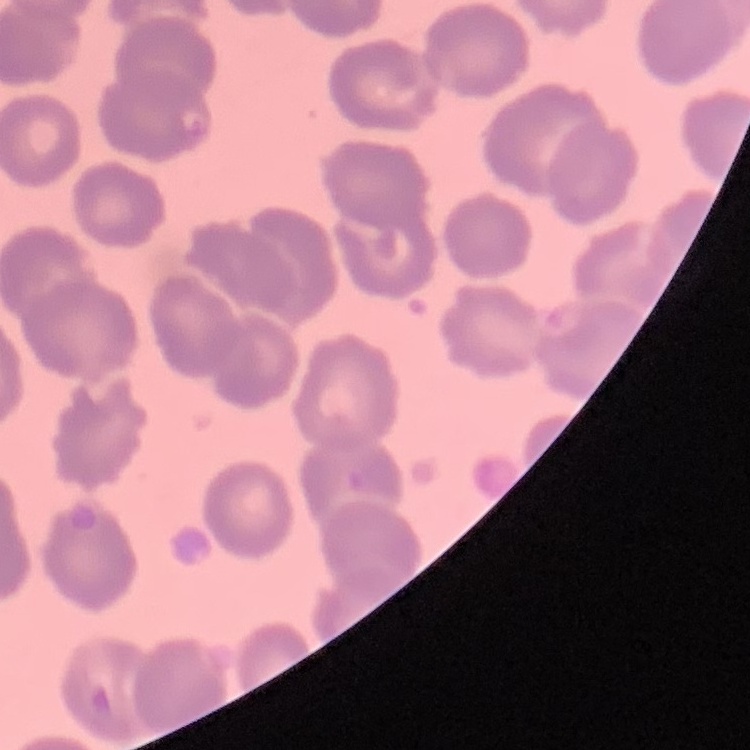

erythrocyte morphology = no rouleaux formation
stain = Field's or Giemsa
image type = one tile cut from a larger photomicrograph
preparation = thin blood film